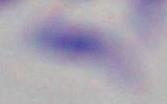

Summary:
  - Identification: Toxoplasma gondii
  - Modality: photomicrograph
  - Magnification: 1000x